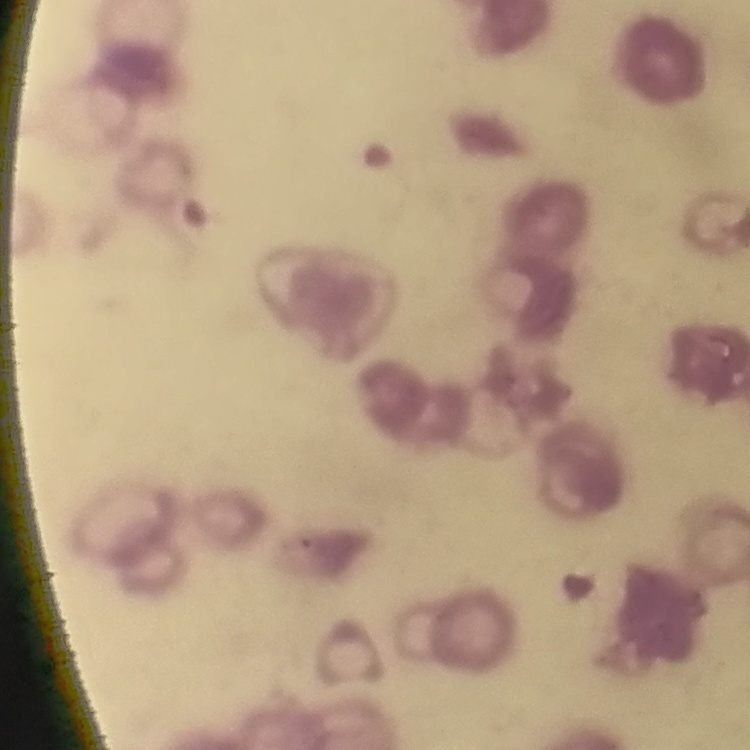

{
  "erythrocyte_morphology": "rouleaux formation",
  "stain": "Field's or Giemsa",
  "image_type": "square crop of a larger photomicrograph",
  "preparation": "thin blood film"
}